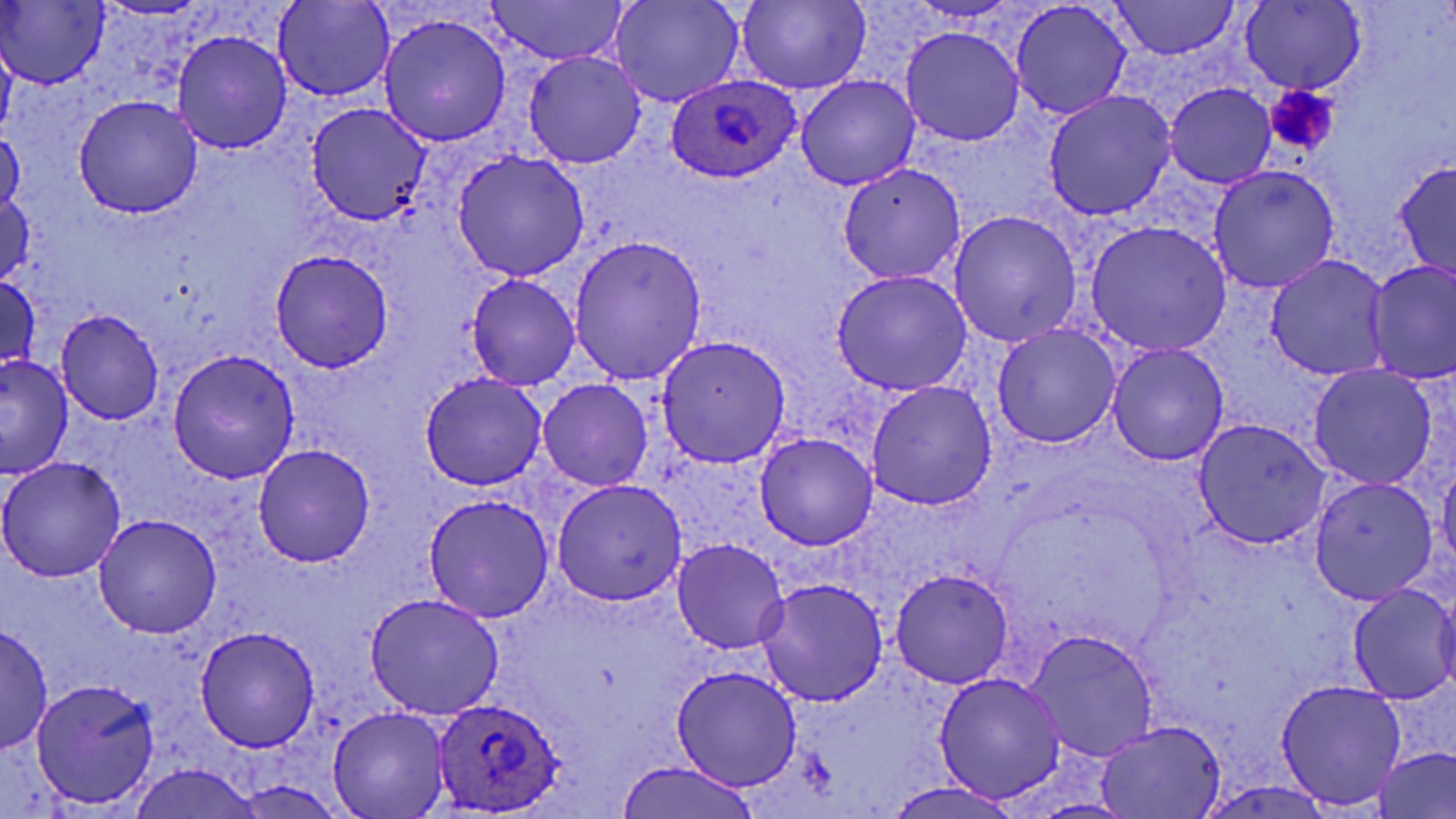

slide-level diagnosis = Plasmodium ovale
stain = May-Grünwald-Giemsa
image size = 1456×819 pixels
uninfected red blood cell locations = approximate bounding boxes as (x1,y1)-(x2,y2) corner pairs in pixels: (485,0)-(629,65), (609,0)-(743,107), (735,0)-(872,95), (1106,0)-(1242,62), (1010,1)-(1133,121), (274,2)-(393,102), (1239,2)-(1366,94), (0,3)-(108,88), (379,14)-(511,146), (901,27)-(1024,146), (172,30)-(291,154), (0,32)-(16,146), (525,51)-(646,167), (795,75)-(919,189), (1165,83)-(1276,188), (1043,90)-(1175,220), (73,96)-(203,218), (306,103)-(432,225), (1,129)-(25,220), (453,151)-(589,281), (1393,160)-(1456,282), (838,163)-(967,284), (1208,166)-(1338,294), (1,193)-(35,288), (949,210)-(1081,347), (1084,222)-(1232,357), (571,234)-(708,384), (269,249)-(394,371), (1265,254)-(1392,381), (1366,262)-(1456,384), (831,270)-(971,395), (464,273)-(580,391), (0,274)-(42,377), (55,309)-(166,425), (993,323)-(1122,449), (656,335)-(790,468), (1107,342)-(1229,466), (168,349)-(300,485), (0,355)-(74,478), (1308,365)-(1438,490), (418,374)-(547,492), (539,378)-(652,491), (866,380)-(997,511), (1194,419)-(1329,548), (755,432)-(877,550), (252,445)-(376,566), (0,456)-(127,580), (1438,461)-(1456,574), (1308,477)-(1438,604), (552,480)-(688,605), (422,494)-(554,623), (92,515)-(221,638), (672,540)-(789,653), (889,567)-(1015,688), (758,578)-(890,704), (1348,583)-(1456,706), (1435,588)-(1456,695), (365,592)-(504,719), (1,622)-(53,755), (196,626)-(320,750), (1025,629)-(1160,760), (669,665)-(802,789), (935,672)-(1066,804), (31,678)-(161,809), (1275,680)-(1407,811), (328,706)-(452,818), (1094,720)-(1224,818), (1373,747)-(1456,817), (613,759)-(765,819), (128,763)-(261,819), (231,777)-(350,818), (1196,778)-(1337,818), (884,780)-(1024,819), (1025,798)-(1139,818)
field of view = one of a larger specimen
preparation = thin blood smear
Plasmodium ovale-infected red blood cell locations = approximate bounding boxes as (x1,y1)-(x2,y2) corner pairs in pixels: (665,74)-(802,182), (432,697)-(566,816)
magnification = 1000x
platelet locations = approximate bounding boxes as (x1,y1)-(x2,y2) corner pairs in pixels: (1264,85)-(1340,155)
modality = optical microscopy